Name the blood parasite species.
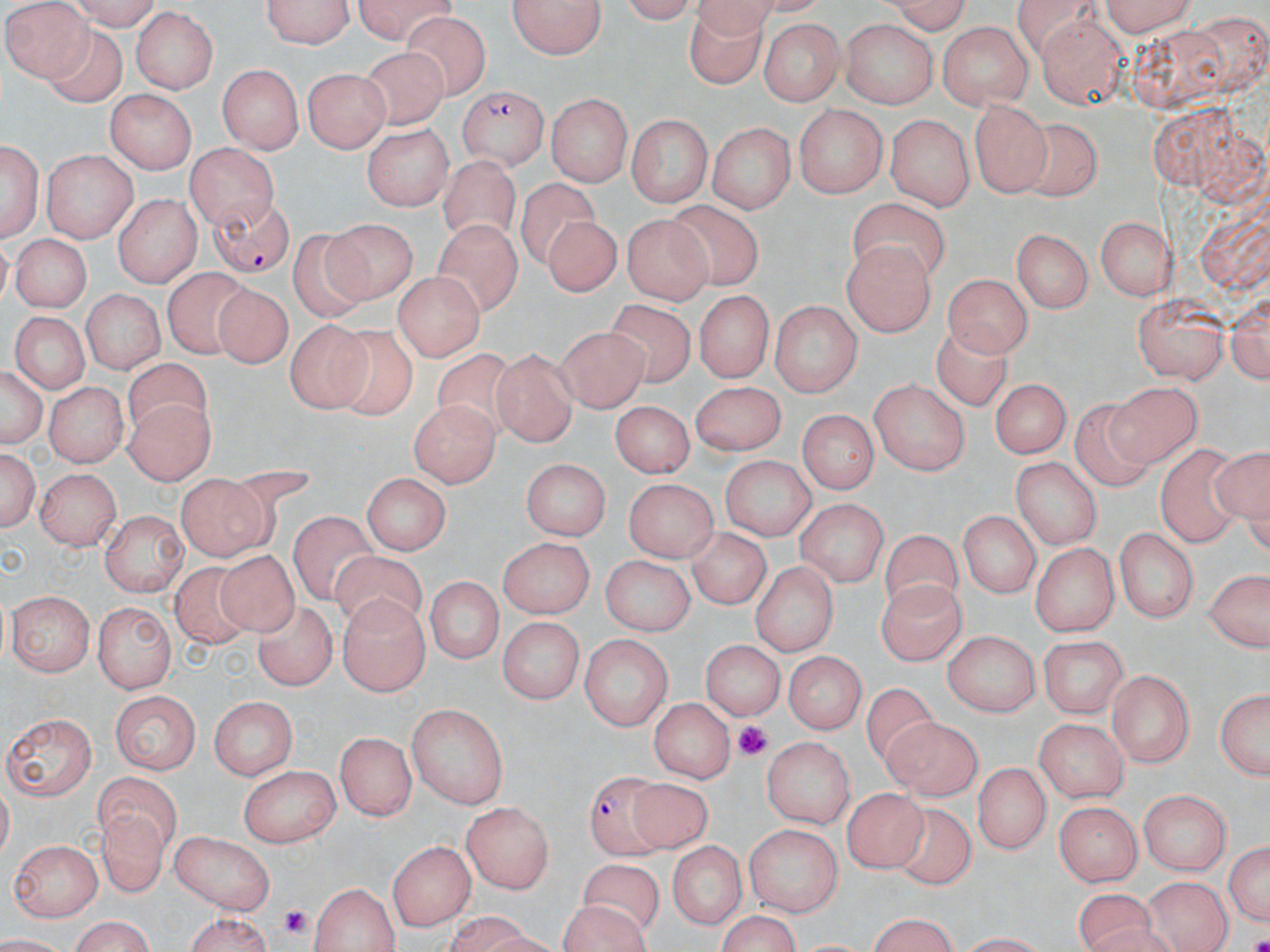

Plasmodium falciparum.

Approximate bounding boxes as named x1/y1/x2/y2 corners in pixels. Plasmodium falciparum-infected red blood cell locations: (x1=459, y1=85, x2=548, y2=170), (x1=202, y1=192, x2=296, y2=277), (x1=582, y1=769, x2=665, y2=858). Platelet locations: (x1=733, y1=719, x2=772, y2=760), (x1=277, y1=903, x2=312, y2=939). Uninfected red blood cell locations: (x1=3, y1=0, x2=94, y2=78), (x1=67, y1=0, x2=159, y2=30), (x1=259, y1=0, x2=357, y2=50), (x1=346, y1=0, x2=457, y2=38), (x1=610, y1=0, x2=703, y2=24), (x1=876, y1=0, x2=975, y2=32), (x1=1094, y1=0, x2=1200, y2=33), (x1=508, y1=1, x2=609, y2=61), (x1=686, y1=2, x2=762, y2=91), (x1=131, y1=7, x2=220, y2=95), (x1=402, y1=10, x2=490, y2=101), (x1=1036, y1=15, x2=1131, y2=110), (x1=758, y1=19, x2=849, y2=104), (x1=842, y1=20, x2=936, y2=107), (x1=937, y1=22, x2=1034, y2=109), (x1=42, y1=26, x2=127, y2=108), (x1=353, y1=44, x2=453, y2=129), (x1=215, y1=64, x2=305, y2=154), (x1=300, y1=69, x2=390, y2=153), (x1=103, y1=89, x2=196, y2=173), (x1=547, y1=92, x2=632, y2=184), (x1=968, y1=97, x2=1050, y2=198), (x1=795, y1=107, x2=885, y2=198), (x1=887, y1=113, x2=974, y2=210), (x1=626, y1=116, x2=714, y2=207), (x1=1018, y1=117, x2=1102, y2=199), (x1=707, y1=120, x2=795, y2=215), (x1=363, y1=126, x2=452, y2=209), (x1=2, y1=134, x2=43, y2=242), (x1=194, y1=142, x2=280, y2=230), (x1=40, y1=148, x2=137, y2=240), (x1=440, y1=155, x2=519, y2=244), (x1=515, y1=175, x2=603, y2=271), (x1=112, y1=193, x2=201, y2=287), (x1=847, y1=197, x2=945, y2=283), (x1=665, y1=200, x2=762, y2=292), (x1=623, y1=213, x2=713, y2=302), (x1=432, y1=214, x2=520, y2=320), (x1=537, y1=215, x2=617, y2=298), (x1=1093, y1=216, x2=1176, y2=300), (x1=326, y1=219, x2=419, y2=307), (x1=286, y1=229, x2=382, y2=319), (x1=1010, y1=229, x2=1093, y2=315), (x1=10, y1=234, x2=96, y2=312), (x1=842, y1=241, x2=934, y2=338), (x1=161, y1=266, x2=253, y2=357), (x1=944, y1=270, x2=1032, y2=357), (x1=391, y1=272, x2=487, y2=358), (x1=209, y1=280, x2=293, y2=374), (x1=81, y1=288, x2=162, y2=378), (x1=1131, y1=290, x2=1228, y2=383), (x1=692, y1=291, x2=772, y2=383), (x1=1225, y1=293, x2=1268, y2=387), (x1=610, y1=297, x2=694, y2=385), (x1=768, y1=301, x2=864, y2=393), (x1=7, y1=312, x2=88, y2=397), (x1=929, y1=317, x2=1013, y2=413), (x1=282, y1=318, x2=366, y2=414), (x1=554, y1=322, x2=647, y2=413), (x1=324, y1=326, x2=416, y2=420), (x1=432, y1=348, x2=523, y2=441), (x1=490, y1=350, x2=579, y2=445), (x1=123, y1=360, x2=218, y2=437), (x1=1, y1=363, x2=46, y2=453), (x1=993, y1=377, x2=1069, y2=460), (x1=869, y1=379, x2=971, y2=476), (x1=44, y1=380, x2=128, y2=467), (x1=689, y1=382, x2=782, y2=455), (x1=1112, y1=382, x2=1199, y2=466), (x1=125, y1=398, x2=212, y2=486), (x1=612, y1=398, x2=694, y2=476), (x1=407, y1=400, x2=500, y2=487), (x1=1070, y1=401, x2=1160, y2=490), (x1=799, y1=408, x2=875, y2=497), (x1=1154, y1=443, x2=1249, y2=548), (x1=1, y1=446, x2=38, y2=533), (x1=1206, y1=447, x2=1268, y2=531), (x1=1012, y1=455, x2=1102, y2=551), (x1=718, y1=456, x2=817, y2=540), (x1=522, y1=457, x2=612, y2=538), (x1=39, y1=466, x2=122, y2=548), (x1=362, y1=471, x2=453, y2=555), (x1=177, y1=476, x2=267, y2=560), (x1=625, y1=479, x2=714, y2=564), (x1=797, y1=497, x2=888, y2=591), (x1=961, y1=508, x2=1041, y2=599), (x1=103, y1=510, x2=187, y2=596), (x1=288, y1=511, x2=379, y2=603), (x1=687, y1=525, x2=771, y2=611), (x1=1115, y1=527, x2=1199, y2=622), (x1=881, y1=530, x2=962, y2=627), (x1=496, y1=539, x2=592, y2=617), (x1=1028, y1=541, x2=1117, y2=634), (x1=217, y1=548, x2=300, y2=637), (x1=326, y1=549, x2=429, y2=635), (x1=600, y1=557, x2=695, y2=638), (x1=748, y1=560, x2=837, y2=659), (x1=173, y1=562, x2=254, y2=650), (x1=1202, y1=569, x2=1270, y2=653), (x1=878, y1=572, x2=964, y2=666), (x1=422, y1=578, x2=504, y2=667), (x1=7, y1=592, x2=94, y2=674), (x1=335, y1=596, x2=429, y2=697), (x1=255, y1=602, x2=335, y2=690), (x1=91, y1=605, x2=179, y2=691), (x1=499, y1=617, x2=583, y2=705), (x1=941, y1=630, x2=1038, y2=716), (x1=579, y1=634, x2=674, y2=727), (x1=1038, y1=637, x2=1129, y2=718), (x1=701, y1=638, x2=781, y2=723), (x1=787, y1=650, x2=867, y2=733), (x1=1107, y1=667, x2=1195, y2=767), (x1=1212, y1=685, x2=1270, y2=784), (x1=860, y1=686, x2=934, y2=764), (x1=107, y1=691, x2=200, y2=773), (x1=648, y1=695, x2=732, y2=785), (x1=210, y1=699, x2=297, y2=778), (x1=406, y1=703, x2=509, y2=810), (x1=4, y1=707, x2=98, y2=801), (x1=877, y1=716, x2=985, y2=802), (x1=1035, y1=716, x2=1129, y2=802), (x1=336, y1=730, x2=415, y2=823), (x1=763, y1=736, x2=857, y2=829), (x1=976, y1=760, x2=1049, y2=856), (x1=240, y1=765, x2=338, y2=844), (x1=91, y1=772, x2=184, y2=851), (x1=628, y1=778, x2=714, y2=848), (x1=844, y1=788, x2=928, y2=873), (x1=1138, y1=789, x2=1229, y2=875), (x1=462, y1=801, x2=556, y2=895), (x1=93, y1=803, x2=170, y2=899), (x1=1052, y1=803, x2=1144, y2=885), (x1=884, y1=804, x2=974, y2=887), (x1=745, y1=825, x2=844, y2=917), (x1=172, y1=832, x2=276, y2=914), (x1=1226, y1=833, x2=1270, y2=930), (x1=390, y1=837, x2=477, y2=929), (x1=9, y1=838, x2=101, y2=922), (x1=666, y1=842, x2=748, y2=932), (x1=579, y1=861, x2=667, y2=935), (x1=1146, y1=875, x2=1230, y2=952), (x1=311, y1=879, x2=400, y2=952), (x1=1072, y1=887, x2=1159, y2=952), (x1=555, y1=900, x2=652, y2=952), (x1=711, y1=912, x2=805, y2=952), (x1=864, y1=915, x2=964, y2=950), (x1=67, y1=916, x2=159, y2=952), (x1=177, y1=916, x2=277, y2=951). Image is 1270×952 pixels. May-Grünwald-Giemsa stain. Optical microscopy. Single field of view. Thin blood film. 1000x magnification.